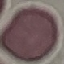

Summary:
  - Malaria status: uninfected
  - Preparation: thin blood film
  - Stain: Giemsa
  - Image type: cell patch, automatically extracted from a larger field of view and resized to 64 × 64 pixels
  - Capture: smartphone through the microscope eyepiece